Give the extent of all Plasmodium falciparum-infected red blood cells.
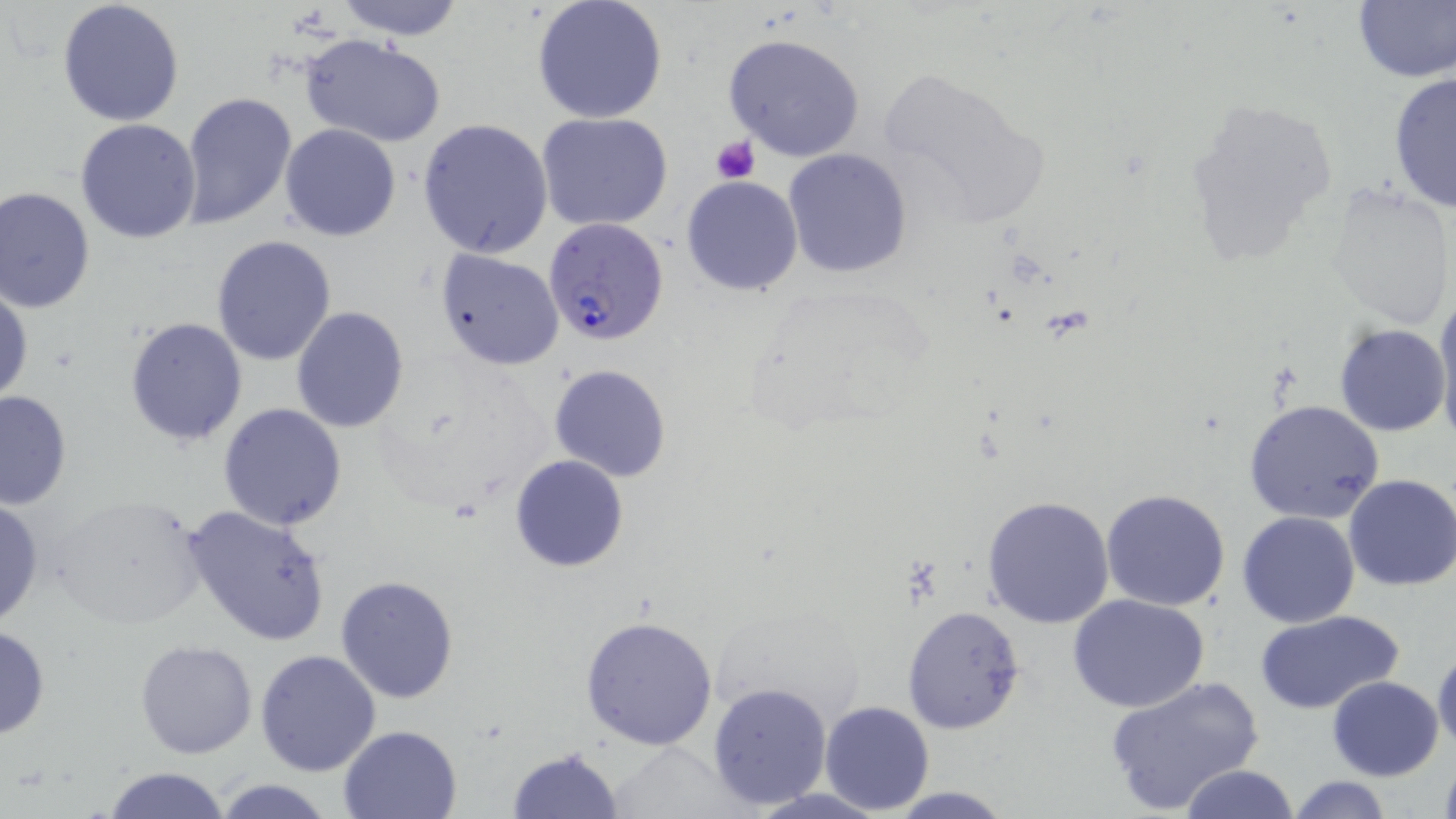
Approximate bounding boxes as [x1, y1, x2, y2] in pixels.
Plasmodium falciparum-infected red blood cells: [542, 218, 669, 346].

slide-level diagnosis = Plasmodium falciparum
preparation = thin blood film
platelet locations = approximate bounding boxes as [x1, y1, x2, y2] in pixels: [710, 136, 760, 184]
modality = optical microscopy
magnification = 1000x
image size = 1456×819 pixels
field of view = single
uninfected red blood cell locations = approximate bounding boxes as [x1, y1, x2, y2] in pixels: [57, 0, 186, 126], [332, 0, 468, 40], [531, 0, 668, 125], [1352, 0, 1456, 83], [722, 32, 865, 161], [301, 34, 447, 148], [877, 70, 1046, 225], [1387, 73, 1455, 215], [1182, 90, 1343, 267], [179, 92, 299, 231], [536, 112, 674, 232], [418, 117, 554, 258], [74, 118, 202, 243], [280, 123, 400, 241], [782, 149, 913, 279], [681, 174, 802, 296], [1325, 184, 1454, 331], [1, 185, 98, 313], [211, 236, 336, 365], [435, 249, 565, 370], [1, 286, 33, 406], [1433, 295, 1456, 441], [290, 308, 409, 432], [124, 315, 248, 447], [1333, 323, 1449, 436], [549, 363, 672, 482], [0, 390, 73, 511], [1243, 398, 1384, 524], [218, 404, 348, 532], [509, 454, 630, 572], [1344, 473, 1456, 592], [1100, 488, 1232, 611], [45, 494, 211, 631], [981, 495, 1117, 630], [0, 499, 45, 630], [182, 503, 333, 647], [1236, 511, 1360, 627], [334, 574, 458, 704], [1067, 592, 1210, 713], [902, 605, 1026, 734], [1253, 611, 1404, 715], [579, 615, 718, 751], [0, 624, 50, 741], [134, 639, 258, 758], [1431, 645, 1456, 755], [255, 649, 382, 777], [1100, 676, 1266, 814], [1327, 676, 1444, 781], [707, 681, 834, 810], [820, 700, 933, 814], [337, 724, 463, 818], [609, 744, 741, 818], [505, 747, 623, 819], [1436, 757, 1456, 819], [1177, 765, 1300, 819], [99, 766, 232, 819], [1286, 775, 1396, 819], [210, 777, 337, 818], [880, 786, 1018, 818], [741, 788, 898, 819]
stain = May-Grünwald-Giemsa